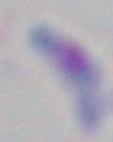
Photomicrograph. Toxoplasma gondii is seen. Captured at 1000x magnification.